Name the parasite shown.
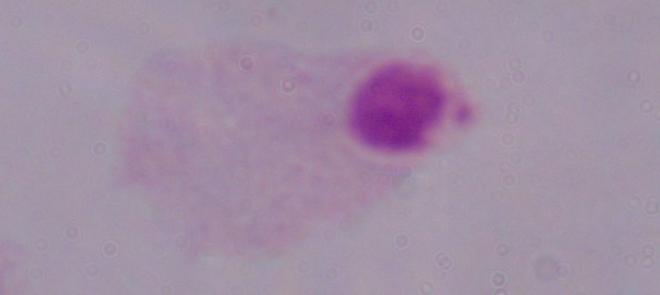

A trichomonad.

magnification = 1000x
modality = photomicrograph